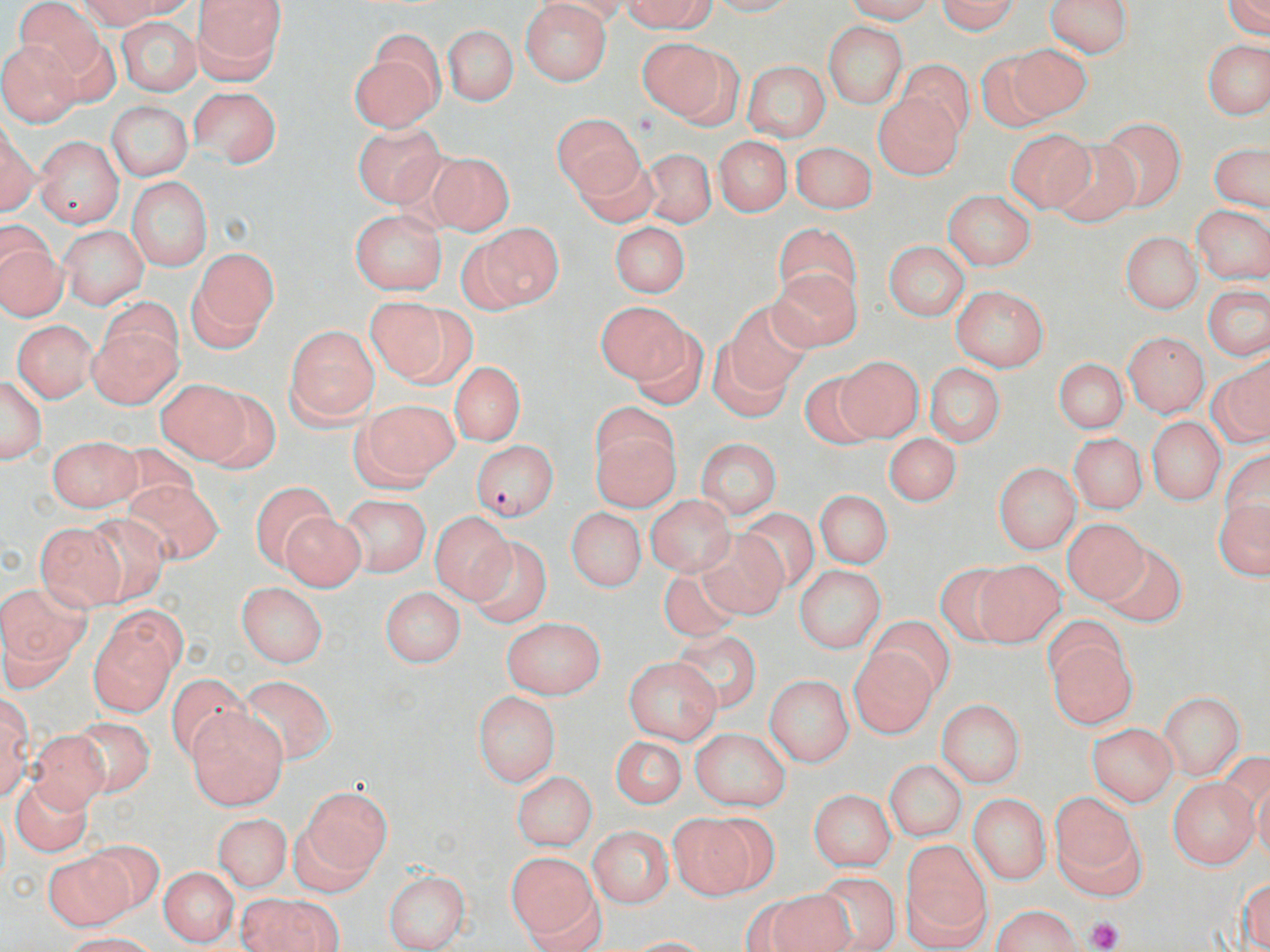

Approximate bounding boxes as named x1/y1/x2/y2 corners in pixels. Platelet locations: (x1=1087, y1=916, x2=1123, y2=949). Plasmodium falciparum-infected red blood cell locations: (x1=471, y1=439, x2=558, y2=519). Uninfected red blood cell locations: (x1=15, y1=0, x2=104, y2=78), (x1=78, y1=0, x2=170, y2=29), (x1=107, y1=0, x2=200, y2=18), (x1=191, y1=0, x2=287, y2=82), (x1=537, y1=0, x2=633, y2=26), (x1=624, y1=0, x2=716, y2=33), (x1=706, y1=0, x2=799, y2=16), (x1=846, y1=0, x2=936, y2=23), (x1=1046, y1=0, x2=1134, y2=57), (x1=1225, y1=0, x2=1270, y2=38), (x1=937, y1=1, x2=1020, y2=34), (x1=520, y1=2, x2=612, y2=85), (x1=116, y1=17, x2=202, y2=96), (x1=823, y1=22, x2=907, y2=107), (x1=444, y1=25, x2=518, y2=105), (x1=639, y1=38, x2=734, y2=123), (x1=1202, y1=40, x2=1270, y2=120), (x1=0, y1=42, x2=81, y2=125), (x1=349, y1=42, x2=442, y2=132), (x1=1004, y1=43, x2=1092, y2=123), (x1=974, y1=51, x2=1056, y2=134), (x1=897, y1=58, x2=975, y2=139), (x1=742, y1=60, x2=831, y2=141), (x1=187, y1=86, x2=282, y2=167), (x1=873, y1=93, x2=963, y2=179), (x1=106, y1=101, x2=192, y2=181), (x1=550, y1=114, x2=645, y2=199), (x1=1096, y1=117, x2=1186, y2=211), (x1=353, y1=122, x2=445, y2=207), (x1=1, y1=126, x2=38, y2=217), (x1=1007, y1=129, x2=1094, y2=212), (x1=35, y1=136, x2=124, y2=229), (x1=714, y1=136, x2=791, y2=216), (x1=1051, y1=138, x2=1140, y2=226), (x1=791, y1=142, x2=877, y2=214), (x1=1209, y1=144, x2=1269, y2=213), (x1=571, y1=146, x2=656, y2=226), (x1=640, y1=148, x2=716, y2=227), (x1=426, y1=151, x2=515, y2=235), (x1=125, y1=178, x2=212, y2=271), (x1=942, y1=189, x2=1036, y2=270), (x1=1191, y1=205, x2=1270, y2=283), (x1=350, y1=209, x2=447, y2=295), (x1=608, y1=221, x2=691, y2=297), (x1=472, y1=222, x2=565, y2=309), (x1=772, y1=224, x2=862, y2=306), (x1=59, y1=226, x2=148, y2=309), (x1=0, y1=232, x2=66, y2=321), (x1=1121, y1=232, x2=1202, y2=314), (x1=883, y1=241, x2=970, y2=321), (x1=190, y1=246, x2=277, y2=345), (x1=769, y1=266, x2=863, y2=353), (x1=951, y1=284, x2=1049, y2=372), (x1=1203, y1=285, x2=1270, y2=360), (x1=364, y1=298, x2=467, y2=387), (x1=596, y1=301, x2=691, y2=389), (x1=723, y1=302, x2=815, y2=391), (x1=13, y1=320, x2=97, y2=402), (x1=88, y1=322, x2=181, y2=408), (x1=626, y1=324, x2=708, y2=410), (x1=285, y1=325, x2=379, y2=425), (x1=1123, y1=331, x2=1210, y2=417), (x1=707, y1=340, x2=795, y2=421), (x1=835, y1=356, x2=923, y2=442), (x1=1210, y1=356, x2=1270, y2=445), (x1=1053, y1=358, x2=1128, y2=434), (x1=450, y1=361, x2=524, y2=446), (x1=924, y1=363, x2=1006, y2=445), (x1=799, y1=370, x2=882, y2=450), (x1=1, y1=376, x2=47, y2=462), (x1=157, y1=378, x2=252, y2=463), (x1=198, y1=389, x2=281, y2=471), (x1=356, y1=399, x2=459, y2=486), (x1=1147, y1=418, x2=1225, y2=506), (x1=592, y1=426, x2=681, y2=513), (x1=884, y1=433, x2=962, y2=507), (x1=1069, y1=433, x2=1147, y2=513), (x1=47, y1=435, x2=140, y2=512), (x1=695, y1=438, x2=782, y2=517), (x1=1219, y1=449, x2=1270, y2=533), (x1=993, y1=463, x2=1081, y2=552), (x1=126, y1=480, x2=223, y2=565), (x1=250, y1=481, x2=336, y2=569), (x1=815, y1=490, x2=893, y2=568), (x1=340, y1=495, x2=430, y2=576), (x1=645, y1=495, x2=735, y2=576), (x1=1212, y1=500, x2=1270, y2=579), (x1=566, y1=507, x2=646, y2=592), (x1=737, y1=508, x2=820, y2=593), (x1=279, y1=510, x2=366, y2=592), (x1=429, y1=512, x2=516, y2=603), (x1=82, y1=514, x2=171, y2=605), (x1=1061, y1=518, x2=1149, y2=605), (x1=34, y1=522, x2=127, y2=610), (x1=696, y1=531, x2=789, y2=620), (x1=465, y1=536, x2=553, y2=629), (x1=1099, y1=542, x2=1187, y2=628), (x1=971, y1=559, x2=1066, y2=647), (x1=656, y1=563, x2=747, y2=642), (x1=933, y1=563, x2=1021, y2=645), (x1=794, y1=565, x2=887, y2=654), (x1=0, y1=581, x2=90, y2=684), (x1=236, y1=582, x2=327, y2=667), (x1=380, y1=587, x2=466, y2=668), (x1=90, y1=612, x2=182, y2=715), (x1=866, y1=615, x2=956, y2=701), (x1=501, y1=617, x2=605, y2=699), (x1=672, y1=630, x2=761, y2=711), (x1=1045, y1=634, x2=1138, y2=731), (x1=850, y1=648, x2=937, y2=736), (x1=624, y1=656, x2=721, y2=745), (x1=165, y1=672, x2=252, y2=763), (x1=765, y1=674, x2=855, y2=766), (x1=237, y1=675, x2=337, y2=766), (x1=472, y1=691, x2=561, y2=786), (x1=1159, y1=692, x2=1245, y2=778), (x1=0, y1=695, x2=33, y2=800), (x1=937, y1=699, x2=1025, y2=786), (x1=189, y1=711, x2=287, y2=810), (x1=68, y1=715, x2=155, y2=797), (x1=1087, y1=722, x2=1178, y2=805), (x1=689, y1=727, x2=791, y2=811), (x1=26, y1=728, x2=109, y2=811), (x1=610, y1=736, x2=687, y2=808), (x1=1220, y1=751, x2=1270, y2=845), (x1=884, y1=759, x2=967, y2=841), (x1=1252, y1=769, x2=1269, y2=863), (x1=512, y1=771, x2=597, y2=851), (x1=1167, y1=777, x2=1259, y2=870), (x1=11, y1=779, x2=93, y2=857), (x1=300, y1=786, x2=392, y2=882), (x1=808, y1=789, x2=897, y2=870), (x1=1051, y1=793, x2=1141, y2=891), (x1=968, y1=794, x2=1051, y2=885), (x1=666, y1=811, x2=762, y2=899), (x1=213, y1=813, x2=292, y2=890), (x1=588, y1=826, x2=673, y2=908), (x1=81, y1=840, x2=165, y2=916), (x1=900, y1=842, x2=992, y2=947), (x1=42, y1=852, x2=131, y2=930), (x1=508, y1=852, x2=597, y2=942), (x1=159, y1=867, x2=239, y2=947), (x1=382, y1=870, x2=471, y2=952), (x1=810, y1=872, x2=902, y2=951), (x1=1236, y1=878, x2=1270, y2=950), (x1=762, y1=889, x2=857, y2=952), (x1=521, y1=891, x2=609, y2=952), (x1=237, y1=894, x2=341, y2=952), (x1=992, y1=904, x2=1085, y2=951), (x1=60, y1=932, x2=157, y2=952), (x1=622, y1=937, x2=717, y2=951). Slide-level diagnosis: Plasmodium falciparum. Image is 1270×952 pixels. 1000x magnification. Thin blood smear. Single field of view. Light microscopy. May-Grünwald-Giemsa stain.